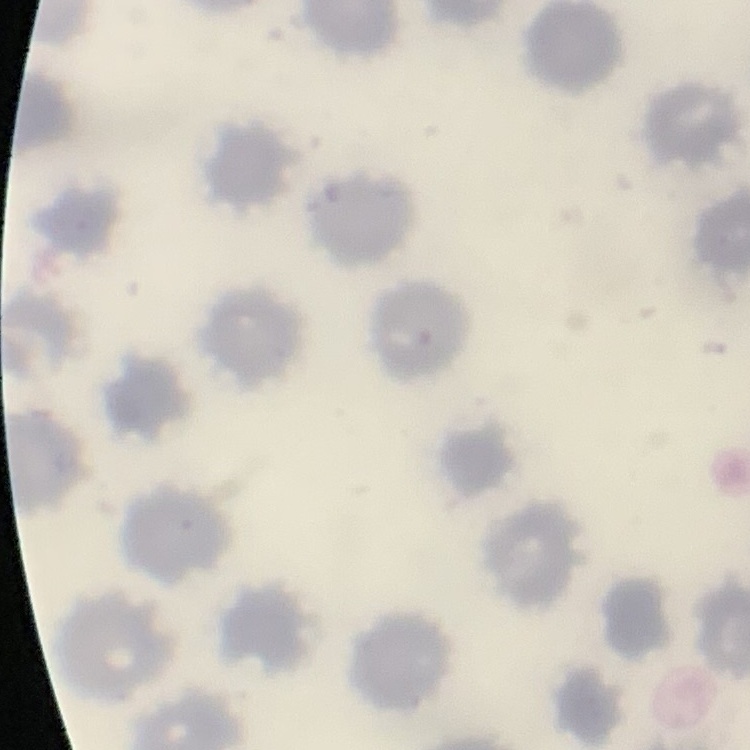

red blood cell morphology = no rouleaux formation
image type = square crop of a larger photomicrograph
stain = Field's or Giemsa
preparation = thin blood film